Assess this cell for malaria.
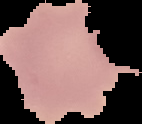
It is uninfected.

Image is 142×124 pixels. Segmented cell region on a black background. From a thin blood film.